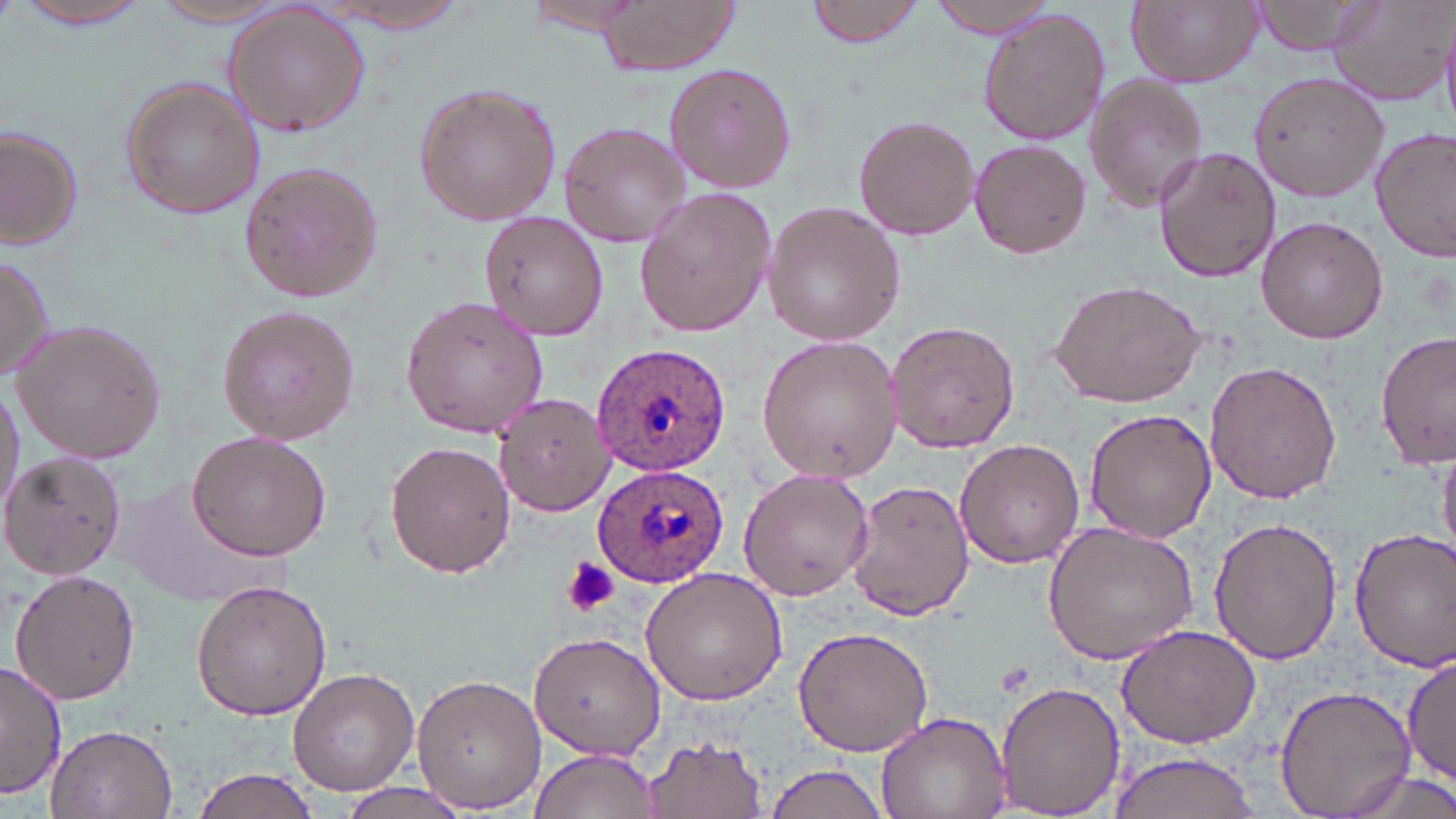

plasmodium_ovale_infected_red_blood_cell_locations: 'approximate bounding boxes as named x1/y1/x2/y2 corners in pixels: (x1=591, y1=343, x2=735, y2=476), (x1=593, y1=462, x2=731, y2=587)'
slide_level_diagnosis: Plasmodium ovale
magnification: 1000x
stain: May-Grünwald-Giemsa
platelet_locations: 'approximate bounding boxes as named x1/y1/x2/y2 corners in pixels: (x1=564, y1=556, x2=619, y2=617)'
image_size: 1456×819 pixels
preparation: thin blood smear
field_of_view: single
modality: optical microscopy
uninfected_red_blood_cell_locations: 'approximate bounding boxes as named x1/y1/x2/y2 corners in pixels: (x1=13, y1=0, x2=154, y2=30), (x1=147, y1=0, x2=300, y2=28), (x1=527, y1=0, x2=652, y2=36), (x1=592, y1=0, x2=737, y2=76), (x1=805, y1=0, x2=926, y2=47), (x1=933, y1=0, x2=1058, y2=39), (x1=1126, y1=0, x2=1260, y2=87), (x1=1248, y1=0, x2=1384, y2=57), (x1=1327, y1=0, x2=1456, y2=107), (x1=312, y1=3, x2=476, y2=35), (x1=220, y1=5, x2=373, y2=138), (x1=978, y1=8, x2=1108, y2=147), (x1=663, y1=61, x2=798, y2=193), (x1=1084, y1=75, x2=1208, y2=213), (x1=1250, y1=75, x2=1388, y2=204), (x1=119, y1=77, x2=265, y2=218), (x1=412, y1=81, x2=561, y2=226), (x1=853, y1=115, x2=981, y2=242), (x1=558, y1=121, x2=690, y2=246), (x1=1, y1=124, x2=82, y2=251), (x1=1371, y1=125, x2=1456, y2=264), (x1=967, y1=139, x2=1092, y2=259), (x1=1153, y1=146, x2=1281, y2=284), (x1=237, y1=160, x2=382, y2=304), (x1=633, y1=187, x2=778, y2=337), (x1=761, y1=201, x2=906, y2=345), (x1=480, y1=212, x2=608, y2=340), (x1=1255, y1=216, x2=1389, y2=345), (x1=0, y1=253, x2=56, y2=381), (x1=1049, y1=277, x2=1209, y2=408), (x1=401, y1=296, x2=551, y2=439), (x1=217, y1=306, x2=364, y2=443), (x1=11, y1=317, x2=166, y2=464), (x1=884, y1=320, x2=1021, y2=453), (x1=1375, y1=328, x2=1455, y2=469), (x1=755, y1=335, x2=903, y2=482), (x1=1203, y1=360, x2=1343, y2=505), (x1=0, y1=381, x2=24, y2=526), (x1=493, y1=392, x2=614, y2=516), (x1=1083, y1=409, x2=1217, y2=544), (x1=188, y1=428, x2=333, y2=560), (x1=954, y1=439, x2=1086, y2=569), (x1=384, y1=440, x2=514, y2=579), (x1=1438, y1=446, x2=1456, y2=562), (x1=1, y1=452, x2=127, y2=580), (x1=738, y1=468, x2=875, y2=602), (x1=845, y1=479, x2=973, y2=624), (x1=1208, y1=516, x2=1343, y2=665), (x1=1042, y1=521, x2=1201, y2=665), (x1=1351, y1=524, x2=1455, y2=674), (x1=9, y1=566, x2=142, y2=705), (x1=641, y1=567, x2=789, y2=705), (x1=190, y1=579, x2=332, y2=721), (x1=1116, y1=623, x2=1263, y2=749), (x1=794, y1=625, x2=936, y2=757), (x1=527, y1=630, x2=665, y2=762), (x1=1401, y1=651, x2=1455, y2=787), (x1=0, y1=661, x2=68, y2=799), (x1=286, y1=665, x2=424, y2=795), (x1=411, y1=673, x2=547, y2=813), (x1=994, y1=679, x2=1126, y2=817), (x1=1274, y1=685, x2=1419, y2=817), (x1=876, y1=711, x2=1009, y2=818), (x1=44, y1=724, x2=178, y2=816), (x1=642, y1=735, x2=769, y2=816), (x1=530, y1=748, x2=660, y2=818), (x1=1106, y1=750, x2=1261, y2=818), (x1=763, y1=762, x2=891, y2=819), (x1=190, y1=767, x2=325, y2=819), (x1=1329, y1=768, x2=1456, y2=819), (x1=335, y1=781, x2=473, y2=818)'